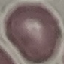

Result: no malaria parasites detected. Thin blood smear. Acquired by smartphone through the microscope eyepiece. Giemsa-stained preparation. Cell patch, automatically extracted from a larger field of view and resized to 64 × 64 pixels.